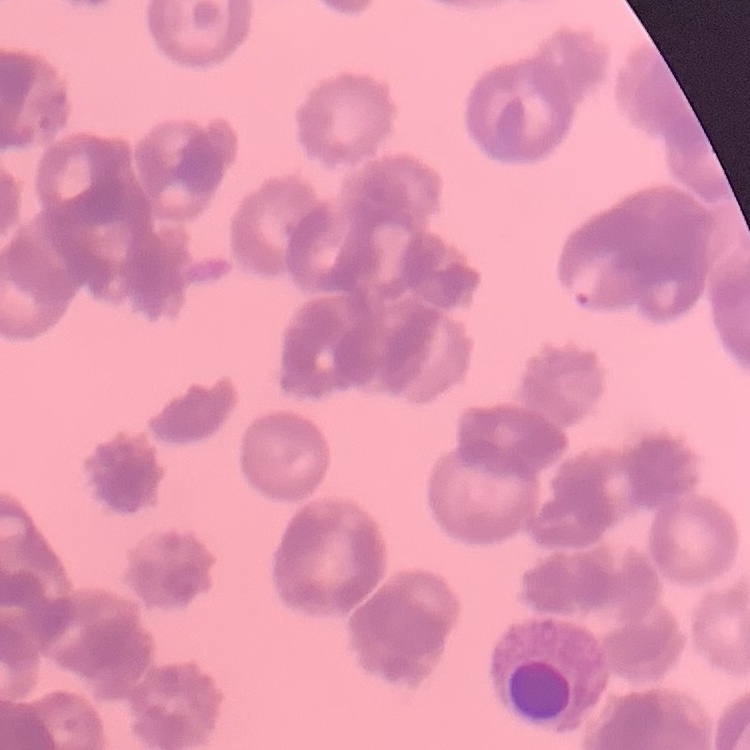

The erythrocytes show rouleaux formation. One tile cut from a larger photomicrograph. Thin blood smear. Stained with either Field's or Giemsa.